Point out each malaria parasite and each leukocyte.
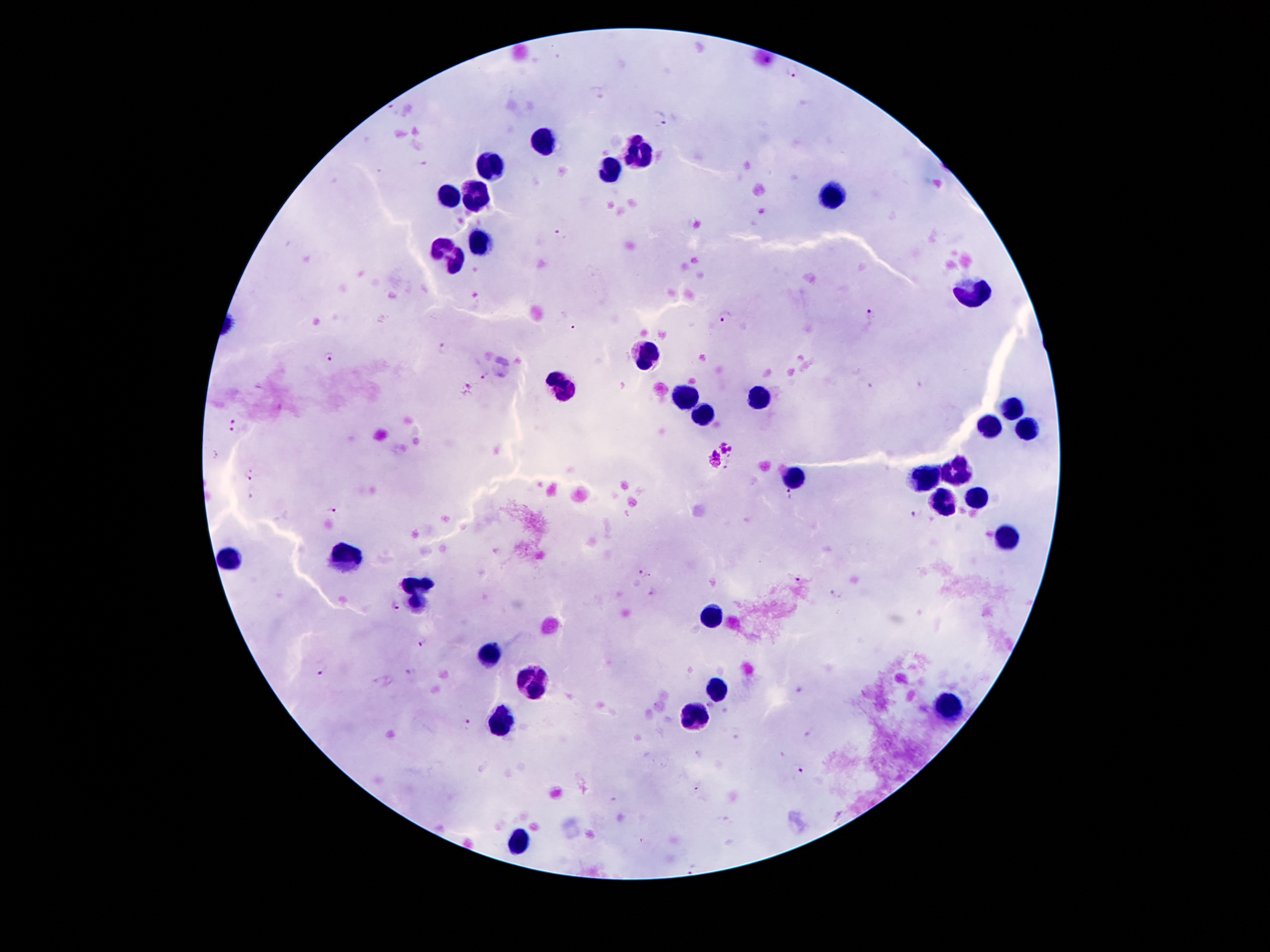

Approximate object centers, in pixels from the top-left corner.
Malaria parasites: (x=793, y=71), (x=393, y=108), (x=661, y=122), (x=559, y=235), (x=870, y=312), (x=725, y=316), (x=574, y=330), (x=444, y=348), (x=329, y=356), (x=484, y=375), (x=469, y=387), (x=235, y=419), (x=235, y=432), (x=249, y=475), (x=252, y=493), (x=792, y=494), (x=331, y=508), (x=918, y=515), (x=641, y=574), (x=797, y=579), (x=835, y=593), (x=395, y=606), (x=423, y=643), (x=319, y=672), (x=798, y=689), (x=468, y=722), (x=800, y=770), (x=699, y=788), (x=694, y=865).
Leukocytes: (x=543, y=142), (x=635, y=150), (x=490, y=165), (x=612, y=170), (x=831, y=193), (x=451, y=194), (x=475, y=195), (x=480, y=241), (x=451, y=251), (x=975, y=295), (x=648, y=355), (x=564, y=387), (x=760, y=396), (x=690, y=399), (x=1011, y=409), (x=703, y=417), (x=989, y=426), (x=1029, y=428), (x=957, y=473), (x=927, y=478), (x=795, y=480), (x=976, y=499), (x=942, y=504), (x=1006, y=538), (x=349, y=558), (x=230, y=561), (x=418, y=592), (x=711, y=617), (x=490, y=656), (x=531, y=684), (x=716, y=686), (x=950, y=707), (x=696, y=718), (x=500, y=725), (x=520, y=843).

stain: Giemsa
capture: smartphone camera through the microscope eyepiece
field_of_view: one from this slide
preparation: thick peripheral-blood smear
image_size: 1270×952 pixels
magnification: 100x
patient_malaria_status: infected with Plasmodium falciparum